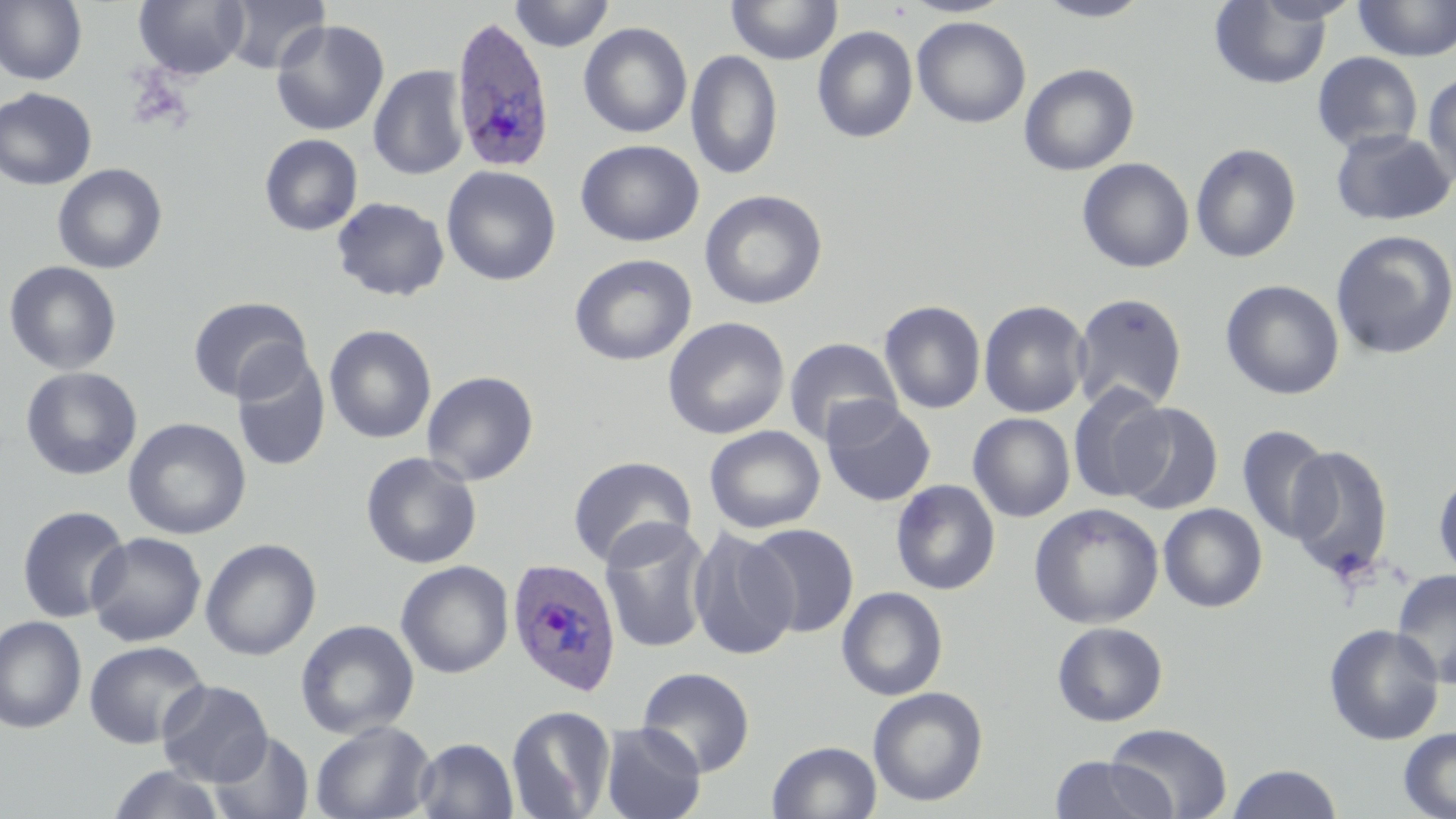

Approximate bounding boxes as (x1, y1, x2, y2) in pixels. Uninfected red blood cell locations: (0, 0, 88, 86), (134, 0, 249, 80), (221, 0, 331, 74), (508, 0, 615, 52), (726, 0, 843, 64), (901, 0, 1014, 18), (1033, 0, 1155, 22), (1209, 1, 1333, 89), (1352, 1, 1456, 61), (911, 16, 1031, 128), (270, 19, 390, 137), (578, 22, 692, 139), (812, 25, 918, 143), (685, 49, 783, 181), (1312, 51, 1423, 154), (1019, 63, 1139, 176), (368, 64, 470, 181), (1422, 71, 1456, 189), (0, 87, 97, 191), (1330, 127, 1455, 226), (259, 134, 364, 236), (576, 140, 704, 247), (1190, 142, 1302, 264), (1076, 157, 1195, 272), (52, 163, 168, 274), (442, 165, 561, 286), (700, 189, 828, 309), (332, 197, 450, 301), (1330, 229, 1456, 360), (569, 254, 697, 366), (3, 260, 122, 375), (1220, 279, 1345, 400), (1071, 293, 1188, 413), (188, 296, 312, 403), (978, 299, 1090, 418), (879, 300, 986, 414), (662, 316, 790, 439), (324, 324, 436, 444), (784, 337, 902, 446), (231, 351, 331, 472), (20, 366, 142, 481), (421, 370, 539, 485), (1068, 383, 1171, 503), (821, 397, 937, 507), (1115, 403, 1223, 515), (968, 413, 1076, 522), (123, 417, 251, 539), (705, 425, 826, 534), (1237, 425, 1333, 544), (1284, 444, 1395, 581), (360, 451, 483, 569), (568, 455, 697, 568), (1433, 468, 1456, 581), (891, 480, 1001, 595), (1028, 503, 1164, 629), (1158, 503, 1268, 612), (16, 504, 132, 623), (599, 517, 713, 655), (746, 522, 860, 637), (687, 526, 798, 661), (86, 531, 207, 647), (200, 538, 322, 661), (395, 560, 514, 679), (1391, 569, 1456, 688), (837, 586, 948, 700), (0, 615, 87, 734), (295, 619, 420, 738), (1051, 621, 1168, 726), (1324, 624, 1443, 745), (84, 640, 210, 749), (637, 666, 755, 777), (157, 679, 274, 786), (868, 686, 988, 807), (506, 704, 616, 819), (310, 720, 436, 819), (599, 723, 706, 819), (1103, 723, 1233, 818), (1399, 727, 1456, 818), (210, 731, 314, 819), (414, 737, 519, 819), (767, 740, 882, 819), (1048, 755, 1175, 819), (1226, 763, 1343, 819), (105, 764, 228, 819). Plasmodium ovale-infected red blood cell locations: (449, 15, 556, 173), (506, 557, 622, 696). Slide-level diagnosis: Plasmodium ovale. Captured at 1000x magnification. May-Grünwald-Giemsa stain. Optical microscopy. Thin blood film. Image is 1456×819 pixels. One field of a larger specimen.